Locate and identify every blood parasite.
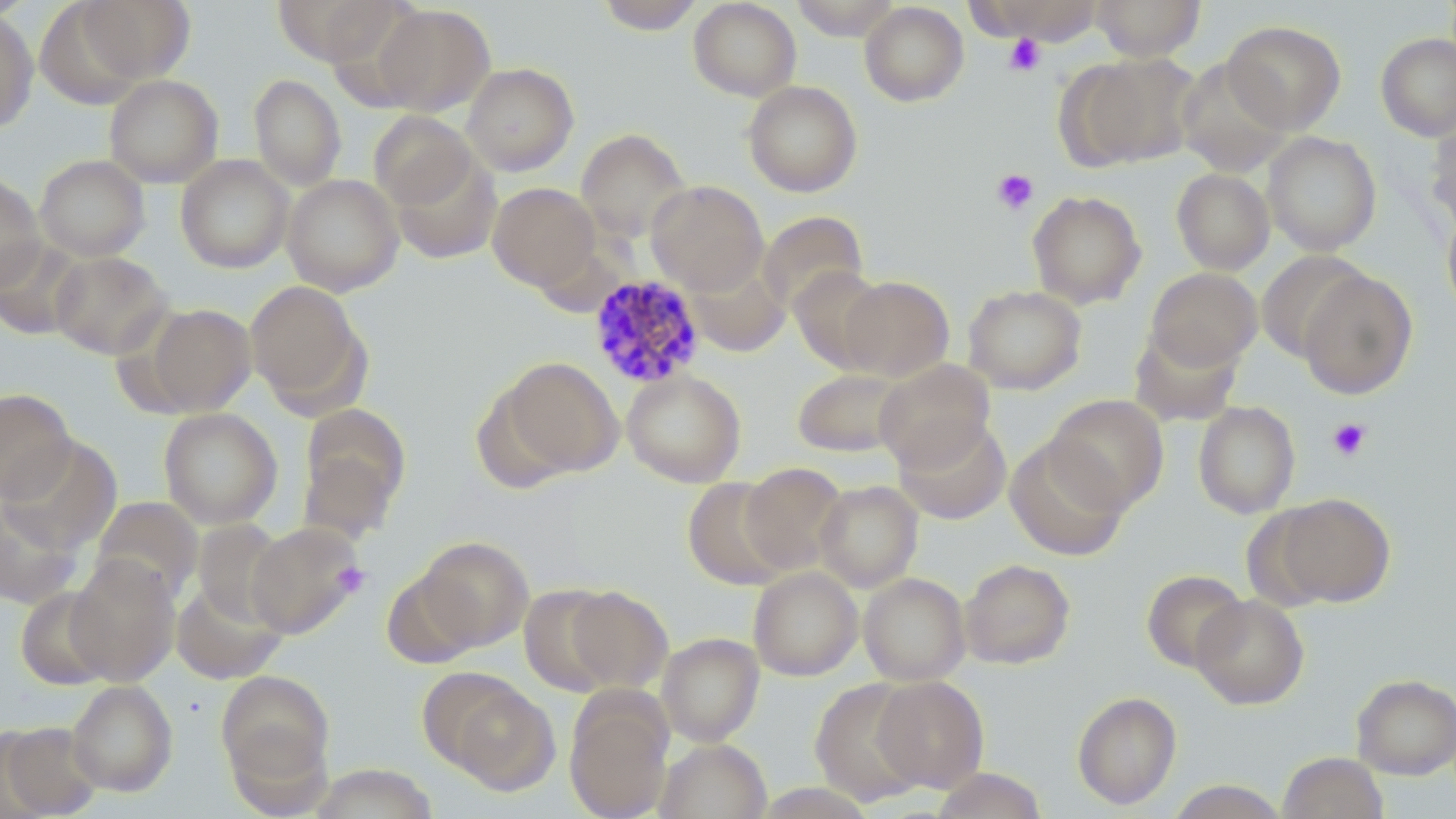
Approximate bounding boxes as (x1, y1, x2, y2) in pixels.
Plasmodium malariae-infected red blood cells: (588, 274, 707, 389).
No Plasmodium falciparum, Plasmodium ovale, Plasmodium vivax, Babesia divergens, or Trypanosoma brucei observed.

slide_level_diagnosis: Plasmodium malariae
image_size: 1456×819 pixels
modality: light microscopy
field_of_view: single
preparation: thin blood smear
stain: May-Grünwald-Giemsa
magnification: 1000x
uninfected_red_blood_cell_locations: 'approximate bounding boxes as (x1, y1, x2, y2) in pixels: (75, 0, 196, 83), (271, 0, 400, 67), (596, 0, 706, 34), (688, 0, 801, 101), (790, 0, 903, 40), (972, 0, 1108, 44), (1091, 0, 1205, 61), (859, 2, 969, 107), (371, 3, 495, 116), (0, 8, 38, 134), (1222, 20, 1346, 134), (1375, 32, 1456, 142), (1064, 52, 1200, 170), (1175, 58, 1293, 175), (462, 62, 579, 176), (103, 74, 223, 188), (249, 74, 346, 190), (743, 80, 862, 197), (369, 111, 477, 210), (1425, 112, 1456, 234), (575, 128, 691, 244), (1262, 131, 1382, 256), (389, 149, 502, 265), (35, 154, 150, 262), (175, 155, 294, 273), (1172, 158, 1374, 265), (1171, 168, 1275, 275), (0, 173, 46, 290), (282, 174, 404, 296), (646, 180, 768, 295), (488, 182, 600, 292), (1027, 191, 1146, 309), (1441, 205, 1456, 321), (757, 210, 868, 315), (0, 237, 88, 340), (50, 251, 173, 359), (1256, 251, 1369, 362), (684, 257, 792, 357), (790, 267, 889, 372), (1146, 267, 1262, 370), (1297, 268, 1418, 400), (839, 276, 954, 382), (245, 280, 366, 410), (963, 285, 1087, 395), (142, 304, 257, 415), (1129, 326, 1242, 426), (495, 357, 623, 480), (873, 359, 996, 471), (791, 368, 910, 458), (621, 369, 746, 487), (0, 388, 75, 503), (1045, 394, 1169, 513), (1192, 400, 1301, 518), (298, 403, 411, 536), (158, 407, 283, 529), (894, 415, 1011, 524), (1005, 436, 1129, 561), (2, 437, 122, 554), (739, 462, 848, 574), (682, 478, 795, 590), (813, 480, 923, 592), (1270, 492, 1395, 608), (91, 496, 203, 604), (0, 498, 83, 608), (193, 519, 292, 625), (246, 522, 367, 638), (414, 536, 534, 651), (65, 554, 180, 686), (960, 559, 1075, 669), (748, 567, 863, 680), (380, 569, 487, 668), (1141, 569, 1248, 672), (858, 572, 970, 686), (171, 580, 288, 684), (519, 583, 625, 697), (562, 585, 673, 693), (15, 586, 118, 690), (1191, 594, 1309, 709), (657, 633, 764, 746), (216, 670, 335, 794), (1352, 673, 1456, 779), (434, 675, 561, 794), (872, 676, 989, 791), (810, 678, 932, 806), (66, 680, 178, 797), (1072, 691, 1182, 809), (565, 693, 673, 819), (0, 721, 103, 818), (655, 738, 771, 819), (1277, 752, 1388, 818), (309, 763, 438, 819), (929, 768, 1048, 818), (1164, 780, 1290, 818)'
platelet_locations: 'approximate bounding boxes as (x1, y1, x2, y2) in pixels: (1004, 34, 1045, 76), (991, 168, 1039, 215), (1327, 417, 1372, 461), (332, 563, 370, 598)'